Outline each Plasmodium falciparum-infected red blood cell.
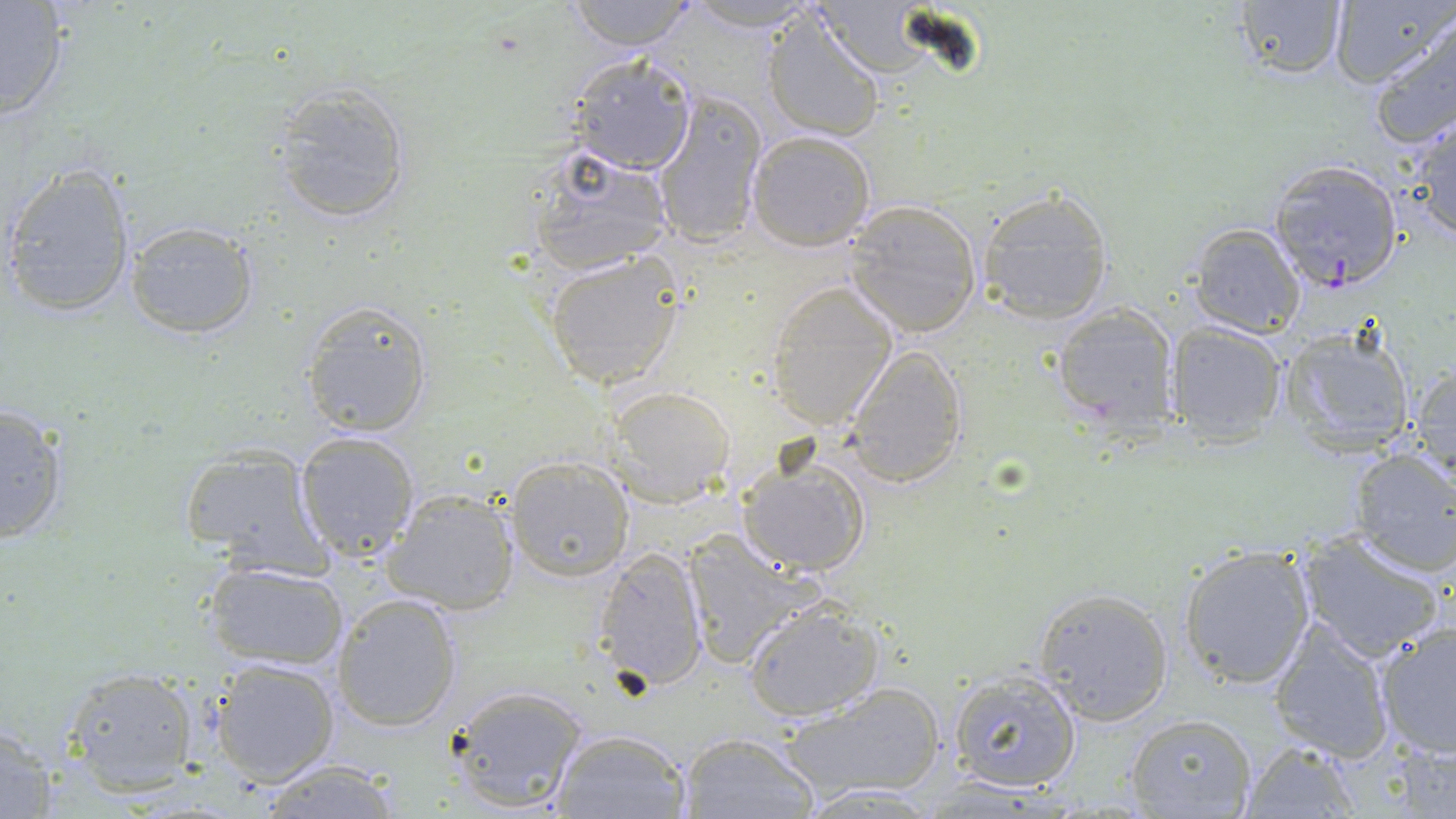

Approximate bounding boxes as named x1/y1/x2/y2 corners in pixels.
Plasmodium falciparum-infected red blood cells: (x1=1266, y1=160, x2=1405, y2=292).

Uninfected red blood cell locations: (x1=562, y1=0, x2=700, y2=51), (x1=1330, y1=0, x2=1453, y2=90), (x1=1230, y1=1, x2=1349, y2=81), (x1=0, y1=2, x2=72, y2=122), (x1=679, y1=2, x2=827, y2=31), (x1=761, y1=8, x2=886, y2=144), (x1=1369, y1=16, x2=1456, y2=151), (x1=566, y1=53, x2=698, y2=175), (x1=270, y1=84, x2=412, y2=223), (x1=650, y1=88, x2=767, y2=249), (x1=1403, y1=112, x2=1456, y2=244), (x1=745, y1=128, x2=877, y2=250), (x1=526, y1=145, x2=675, y2=276), (x1=3, y1=161, x2=138, y2=317), (x1=974, y1=189, x2=1113, y2=325), (x1=843, y1=200, x2=983, y2=338), (x1=122, y1=219, x2=261, y2=338), (x1=1189, y1=222, x2=1305, y2=336), (x1=544, y1=251, x2=683, y2=388), (x1=764, y1=280, x2=900, y2=432), (x1=300, y1=299, x2=435, y2=438), (x1=1051, y1=305, x2=1179, y2=433), (x1=1165, y1=322, x2=1286, y2=444), (x1=1278, y1=328, x2=1418, y2=455), (x1=841, y1=344, x2=969, y2=488), (x1=1408, y1=360, x2=1456, y2=488), (x1=604, y1=385, x2=735, y2=507), (x1=0, y1=403, x2=71, y2=545), (x1=292, y1=430, x2=422, y2=561), (x1=178, y1=443, x2=329, y2=576), (x1=1346, y1=448, x2=1456, y2=577), (x1=737, y1=454, x2=870, y2=576), (x1=503, y1=455, x2=635, y2=583), (x1=381, y1=490, x2=519, y2=615), (x1=1296, y1=531, x2=1448, y2=663), (x1=681, y1=533, x2=817, y2=671), (x1=1177, y1=544, x2=1316, y2=689), (x1=594, y1=546, x2=711, y2=693), (x1=202, y1=560, x2=349, y2=672), (x1=1034, y1=588, x2=1173, y2=723), (x1=331, y1=593, x2=462, y2=731), (x1=741, y1=600, x2=884, y2=719), (x1=1269, y1=620, x2=1398, y2=760), (x1=1375, y1=622, x2=1456, y2=757), (x1=211, y1=658, x2=340, y2=786), (x1=60, y1=666, x2=200, y2=790), (x1=946, y1=668, x2=1083, y2=791), (x1=444, y1=682, x2=590, y2=813), (x1=783, y1=683, x2=948, y2=800), (x1=1124, y1=713, x2=1259, y2=817), (x1=0, y1=725, x2=61, y2=818), (x1=550, y1=728, x2=691, y2=818), (x1=677, y1=731, x2=818, y2=817), (x1=1239, y1=738, x2=1362, y2=816), (x1=255, y1=760, x2=404, y2=818), (x1=797, y1=782, x2=944, y2=816). Slide-level diagnosis: Plasmodium falciparum. One field of a larger specimen. Thin blood smear. May-Grünwald-Giemsa stain. Captured at 1000x magnification. Image is 1456×819 pixels. Optical microscopy.